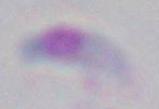

identification = Toxoplasma gondii
magnification = 1000x
modality = micrograph